Locate and identify every blood parasite.
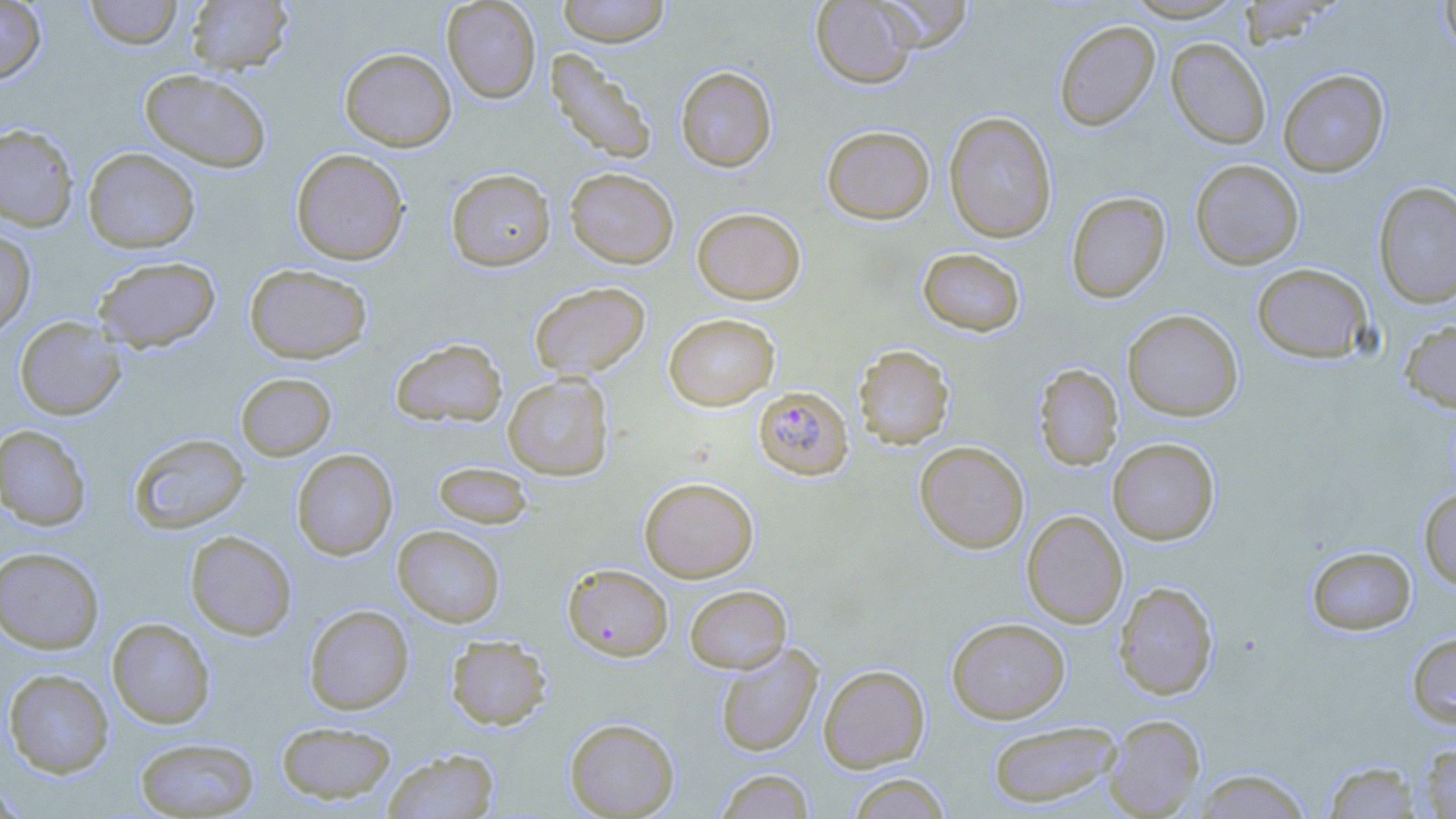
Approximate bounding boxes as [x1, y1, x2, y2] in pixels.
Plasmodium falciparum-infected red blood cells: [753, 385, 853, 481].
No Plasmodium ovale, Plasmodium malariae, Plasmodium vivax, Babesia divergens, or Trypanosoma brucei observed.

slide-level diagnosis = Plasmodium falciparum
magnification = 1000x
field of view = single
image size = 1456×819 pixels
uninfected red blood cell locations = approximate bounding boxes as [x1, y1, x2, y2] in pixels: [0, 0, 45, 84], [84, 0, 183, 49], [186, 0, 292, 76], [442, 0, 542, 103], [557, 0, 670, 47], [811, 0, 919, 89], [876, 0, 972, 52], [1123, 0, 1247, 22], [1439, 0, 1456, 58], [1237, 1, 1334, 48], [1054, 19, 1159, 131], [1166, 37, 1271, 149], [339, 47, 456, 151], [545, 48, 657, 165], [676, 66, 777, 172], [139, 68, 272, 172], [1277, 68, 1389, 177], [943, 111, 1057, 243], [0, 123, 79, 231], [821, 124, 935, 224], [83, 147, 200, 253], [290, 148, 410, 265], [1190, 159, 1304, 270], [446, 168, 556, 272], [565, 168, 679, 269], [1372, 181, 1456, 309], [1065, 191, 1170, 303], [692, 207, 806, 304], [0, 229, 36, 338], [917, 247, 1026, 337], [93, 256, 221, 352], [244, 263, 372, 364], [1252, 263, 1373, 363], [529, 281, 650, 380], [1122, 309, 1243, 421], [663, 313, 780, 411], [15, 316, 125, 420], [1398, 319, 1456, 414], [390, 338, 507, 428], [853, 344, 955, 449], [1033, 363, 1123, 471], [235, 372, 337, 461], [503, 374, 614, 481], [0, 425, 92, 530], [129, 433, 249, 534], [1107, 438, 1220, 544], [914, 441, 1029, 553], [292, 449, 398, 560], [433, 461, 533, 529], [639, 476, 758, 582], [1419, 487, 1456, 590], [1022, 510, 1127, 628], [393, 525, 505, 627], [185, 531, 297, 641], [1306, 545, 1416, 635], [0, 547, 105, 654], [562, 563, 673, 661], [1113, 581, 1218, 700], [685, 585, 792, 674], [304, 604, 414, 714], [107, 617, 215, 728], [947, 617, 1070, 723], [1407, 630, 1456, 728], [446, 634, 552, 730], [715, 642, 823, 757], [818, 664, 930, 772], [3, 668, 114, 778], [1103, 714, 1205, 818], [565, 717, 680, 817], [988, 719, 1122, 809], [276, 721, 397, 804], [135, 737, 259, 817], [1418, 741, 1456, 818], [383, 749, 499, 819], [1323, 760, 1423, 818], [1192, 768, 1312, 818], [715, 769, 814, 818], [847, 772, 952, 818], [0, 777, 26, 817]
preparation = thin blood smear
stain = May-Grünwald-Giemsa
modality = optical microscopy